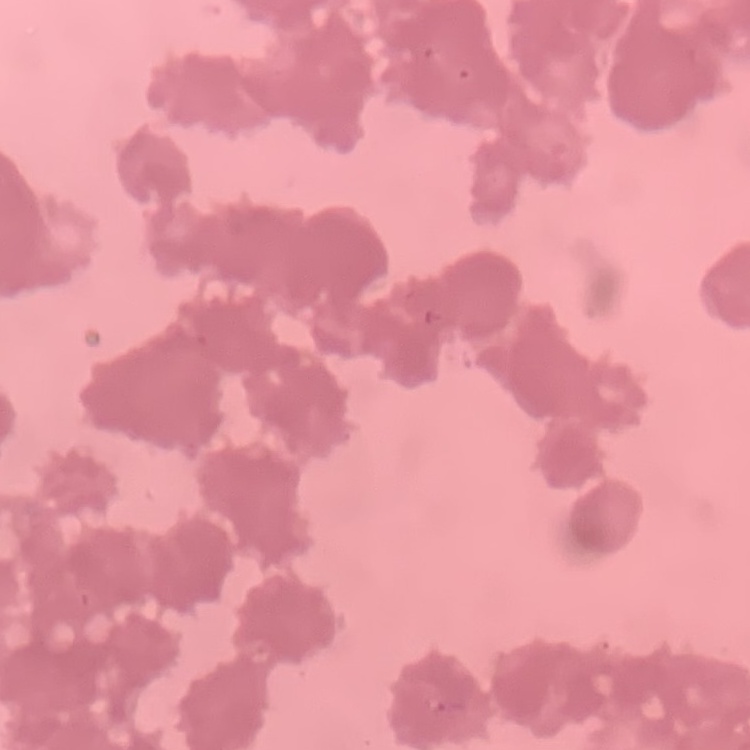

erythrocyte morphology = rouleaux formation
image type = square crop of a larger photomicrograph
preparation = thin blood film
stain = Field's or Giemsa